Describe the morphology of the red blood cells.
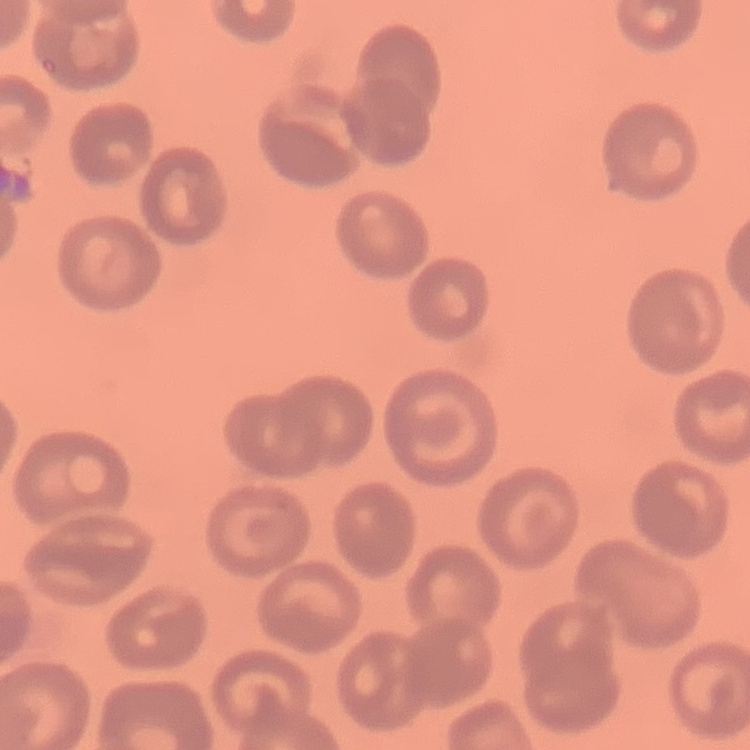

They show no rouleaux formation.

preparation = thin blood smear
image type = square crop of a larger photomicrograph
stain = Field's or Giemsa